Give the extent of all Trypanosoma brucei.
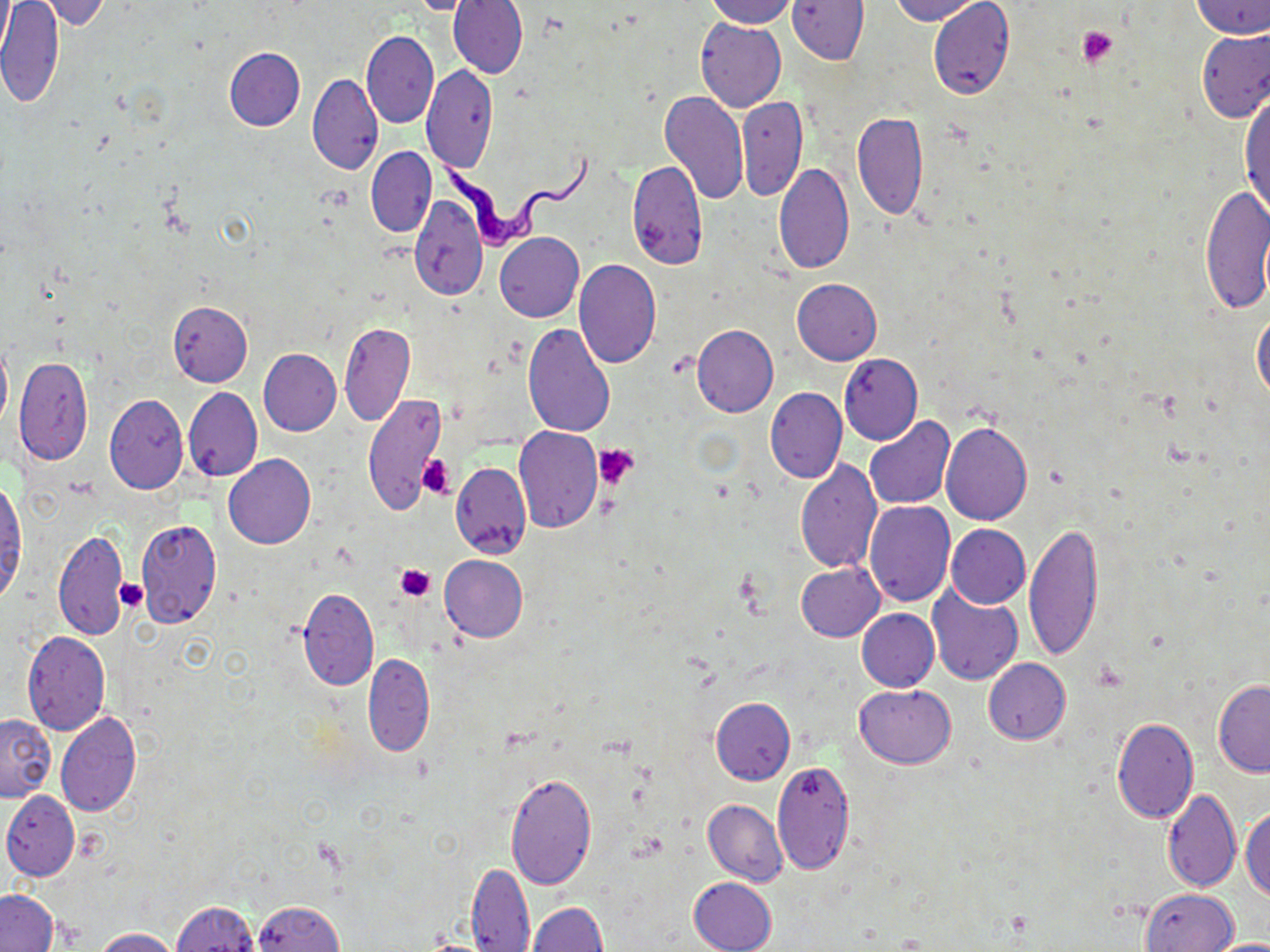

Approximate bounding boxes as [x1, y1, x2, y2] in pixels.
Trypanosoma brucei: [429, 143, 599, 253].

Uninfected red blood cell locations: [35, 0, 113, 31], [409, 0, 478, 15], [449, 0, 527, 79], [704, 0, 796, 27], [787, 0, 869, 64], [889, 0, 986, 24], [927, 0, 1015, 102], [1189, 0, 1270, 40], [0, 1, 65, 108], [695, 19, 786, 112], [1197, 28, 1270, 123], [361, 30, 439, 129], [224, 48, 305, 131], [423, 64, 497, 173], [307, 73, 382, 175], [1239, 88, 1269, 224], [658, 92, 749, 204], [737, 94, 809, 200], [852, 111, 927, 219], [366, 147, 437, 238], [628, 160, 707, 270], [773, 162, 855, 276], [1199, 181, 1270, 313], [410, 194, 487, 301], [494, 232, 584, 322], [573, 259, 660, 368], [792, 278, 882, 366], [167, 301, 252, 386], [1252, 309, 1270, 402], [340, 322, 414, 428], [523, 322, 614, 437], [692, 324, 779, 416], [0, 337, 12, 433], [257, 349, 341, 436], [838, 353, 923, 445], [14, 356, 93, 465], [184, 386, 262, 481], [764, 386, 846, 483], [362, 393, 447, 516], [104, 395, 188, 495], [864, 416, 956, 511], [941, 422, 1033, 525], [513, 426, 603, 532], [223, 454, 316, 549], [793, 457, 882, 574], [451, 461, 531, 558], [804, 479, 945, 592], [0, 480, 26, 600], [863, 500, 955, 607], [136, 519, 221, 628], [1023, 521, 1102, 662], [945, 524, 1030, 608], [53, 528, 128, 641], [439, 555, 528, 642], [796, 562, 885, 642], [927, 583, 1023, 685], [298, 588, 379, 690], [857, 608, 939, 691], [22, 630, 110, 735], [363, 653, 435, 756], [984, 658, 1071, 745], [1213, 680, 1270, 777], [855, 684, 955, 768], [710, 697, 795, 785], [56, 711, 142, 817], [1, 713, 55, 801], [1111, 717, 1198, 822], [772, 758, 856, 875], [504, 770, 597, 891], [1162, 787, 1239, 890], [2, 791, 80, 881], [703, 798, 788, 885], [1242, 805, 1270, 902], [467, 862, 535, 951], [689, 876, 777, 952], [1142, 888, 1239, 952], [0, 890, 57, 952], [252, 900, 344, 952], [173, 901, 260, 952], [528, 903, 607, 952], [92, 927, 179, 951], [1203, 936, 1270, 952]. Platelet locations: [1078, 26, 1117, 66], [593, 444, 638, 487], [416, 455, 453, 498], [395, 564, 435, 601], [115, 580, 150, 613]. Slide-level diagnosis: Trypanosoma brucei. Optical microscopy. Single field of view. Image is 1270×952 pixels. 1000x magnification. May-Grünwald-Giemsa stain. Thin blood film.